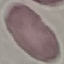

malaria status = uninfected
image type = automatically extracted cell patch, resized to 64 × 64 pixels
preparation = thin blood smear
stain = Giemsa
capture = smartphone through the microscope eyepiece